Report the malaria status of this cell.
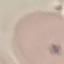
Uninfected.

image_type: cell patch, automatically extracted from a larger field of view and resized to 64 × 64 pixels
preparation: thin blood smear
capture: smartphone through the microscope eyepiece
stain: Giemsa